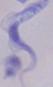

Photomicrograph. 1000x magnification. A trypanosome is shown.